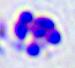

modality: micrograph
magnification: 400x
identification: leukocyte